Comment on the morphology of the red blood cells.
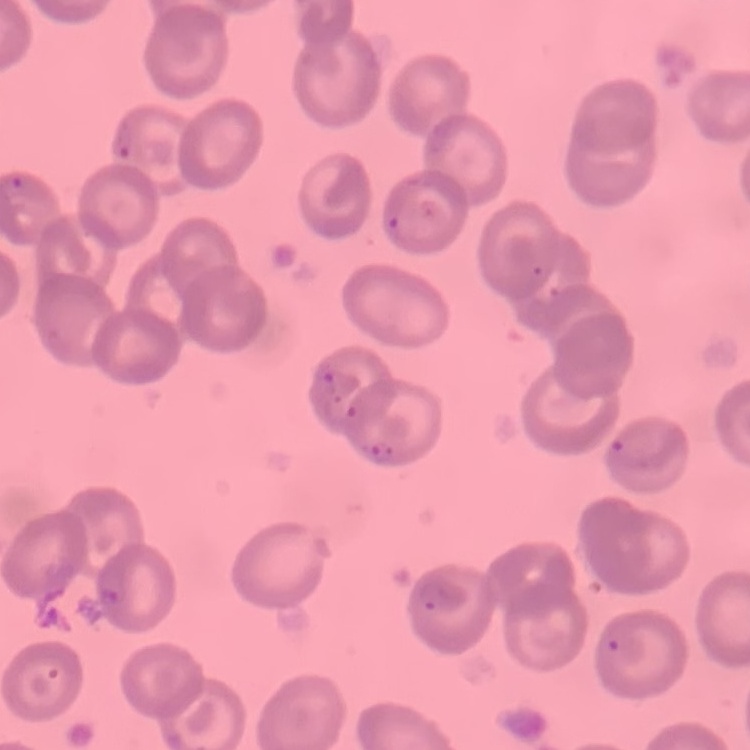
They show no rouleaux formation.

{
  "preparation": "thin blood smear",
  "image_type": "one tile cut from a larger photomicrograph",
  "stain": "Field's or Giemsa"
}